Evaluate for parasitized red blood cells.
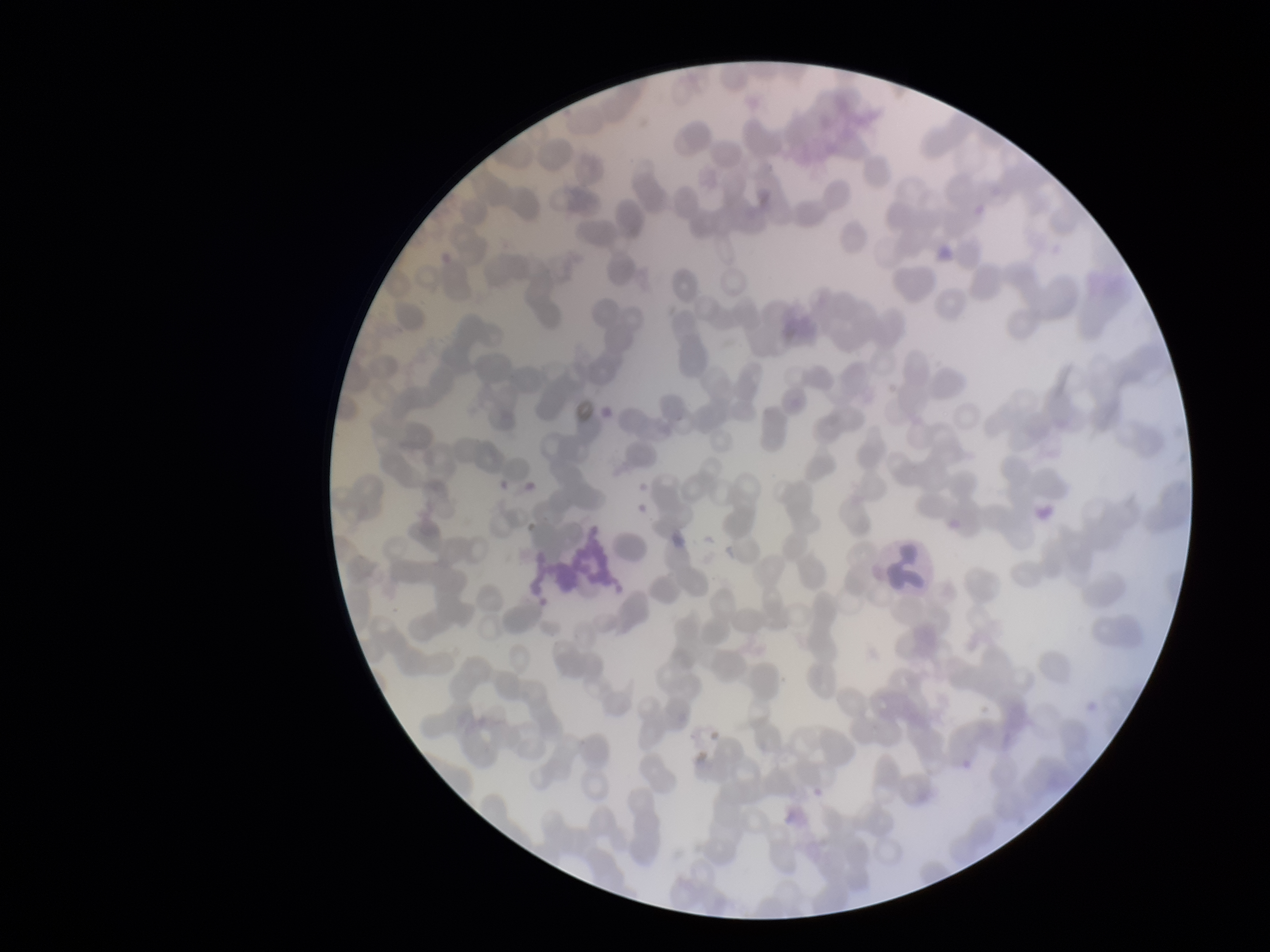

None detected.

Summary:
  - Field of view: one from this slide
  - Patient malaria status: negative
  - Red blood cell count: 270
  - Preparation: thin
  - Image size: 1270×952 pixels
  - Capture: smartphone photograph through the microscope eyepiece
  - Parasitized red blood cell count: 0
  - Stain: Giemsa